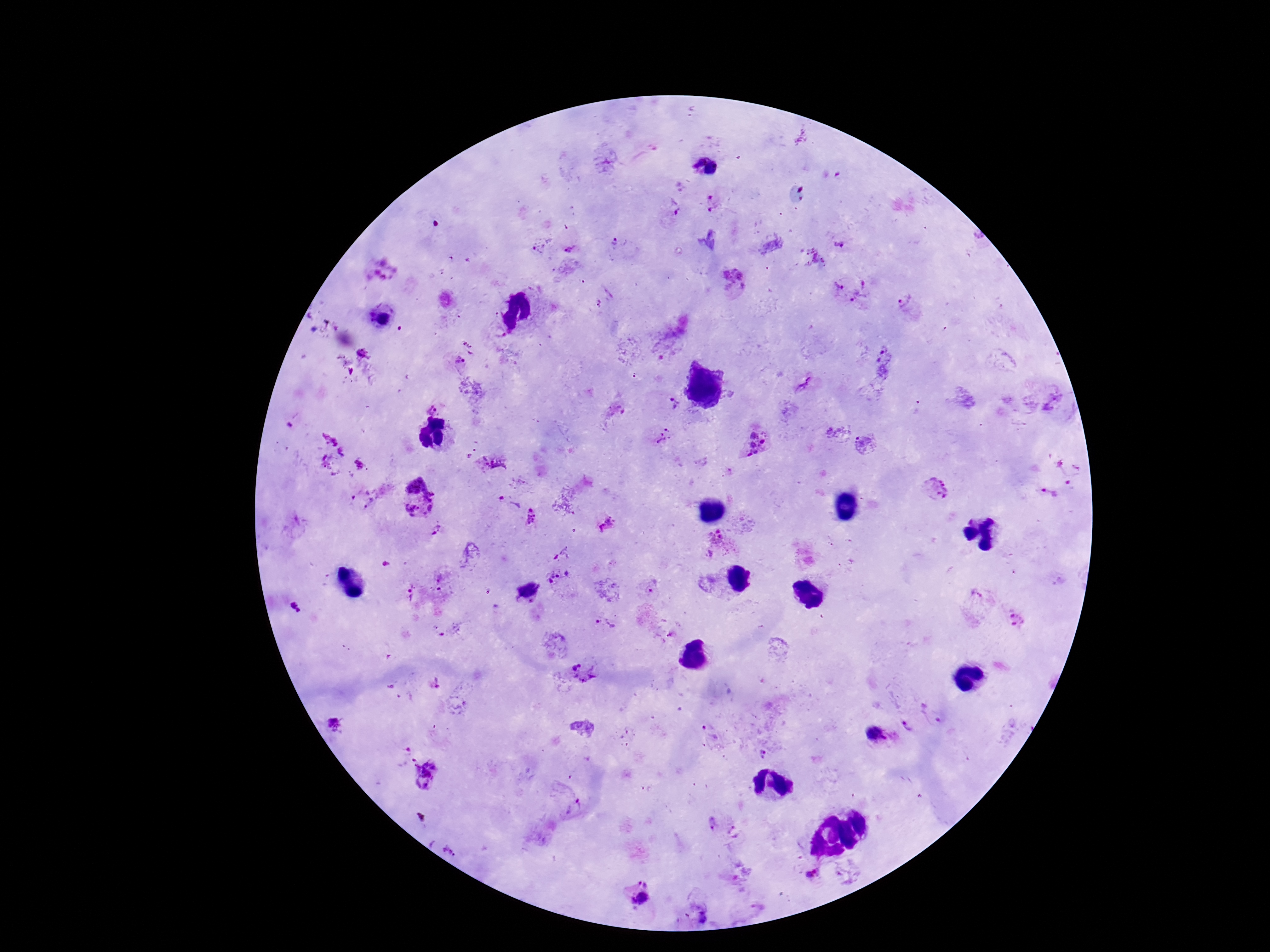
Approximate centers as (x, y) in pixels.
Summary:
  - Plasmodium parasite locations: (694, 158), (715, 169), (715, 202), (673, 207), (613, 241), (841, 242), (570, 244), (540, 249), (736, 282), (837, 287), (864, 295), (901, 300), (379, 312), (467, 344), (363, 353), (459, 363), (884, 364), (804, 387), (431, 407), (671, 407), (664, 438), (476, 445), (758, 445), (468, 457), (494, 465), (361, 466), (414, 480), (937, 488), (1048, 494), (361, 499), (423, 506), (530, 516), (608, 523), (436, 529), (718, 545), (561, 580), (655, 588), (528, 592), (977, 597), (296, 608), (1017, 621), (605, 625), (583, 671), (335, 724), (907, 726), (878, 735), (404, 748), (426, 773), (576, 806), (710, 823), (734, 833), (811, 873), (635, 892)
  - Preparation: thick blood smear
  - Capture: smartphone camera through the microscope eyepiece
  - Magnification: 100x
  - Patient malaria status: infected
  - Image size: 1270×952 pixels
  - Stain: Giemsa
  - Field of view: single